Name the parasite shown.
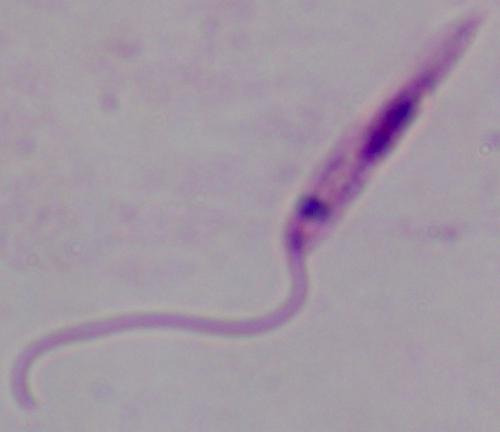
Leishmania.

Photomicrograph. Captured at 1000x magnification.